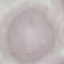
Malaria status: uninfected. Thin blood film. Photographed with a smartphone camera at the microscope eyepiece. Giemsa-stained preparation. Cell patch, automatically extracted from a larger field of view and resized to 64 × 64 pixels.